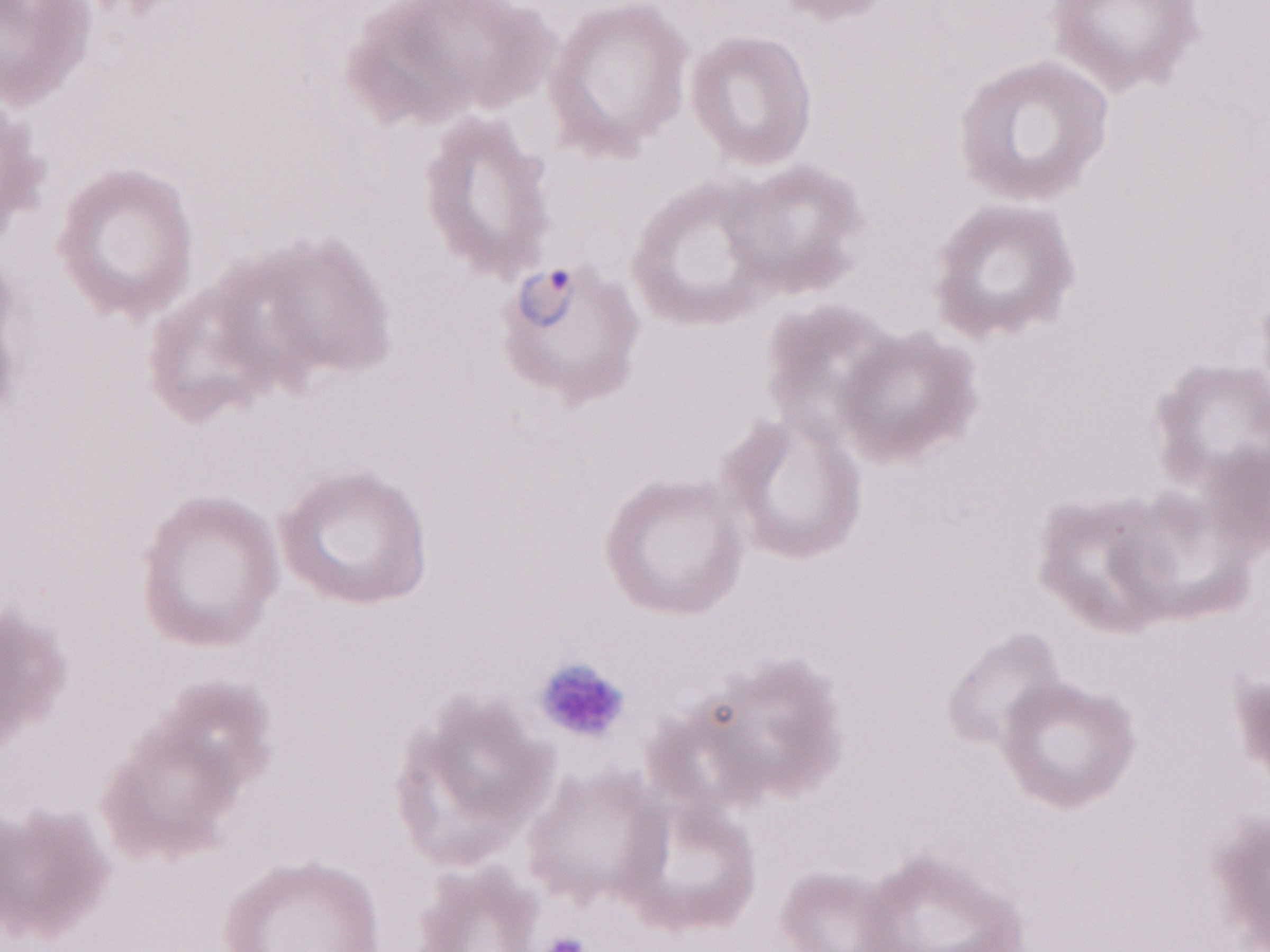 Patient-level malaria diagnosis: positive. Olympus BX43 microscope and DP73 digital camera. May-Grünwald-Giemsa-stained preparation. Thin peripheral-blood smear. Single field of view. 1,000x magnification. Image is 1270×952 pixels.